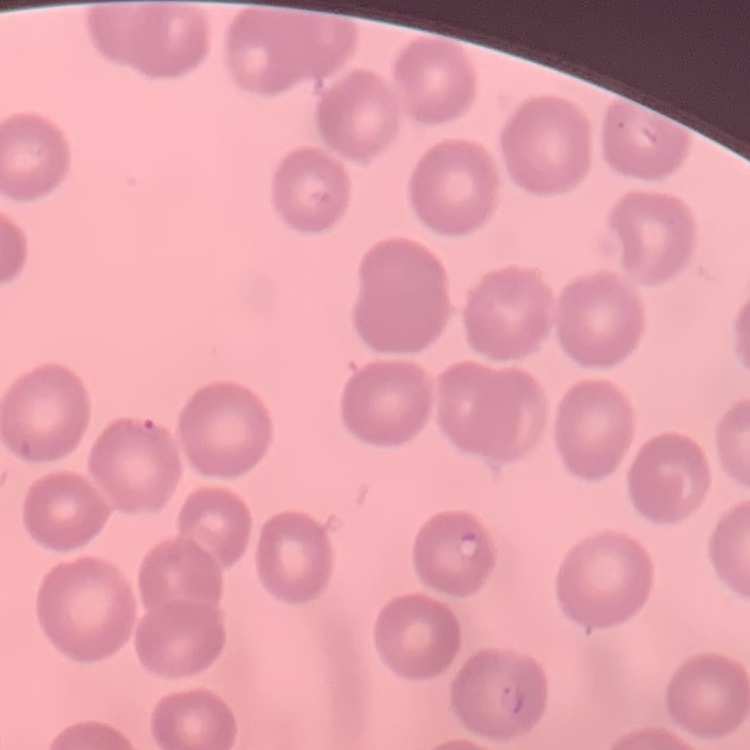

red blood cell morphology = no rouleaux formation
preparation = thin peripheral smear
image type = one tile cut from a larger photomicrograph
stain = Field's or Giemsa